Identify the preparation type.
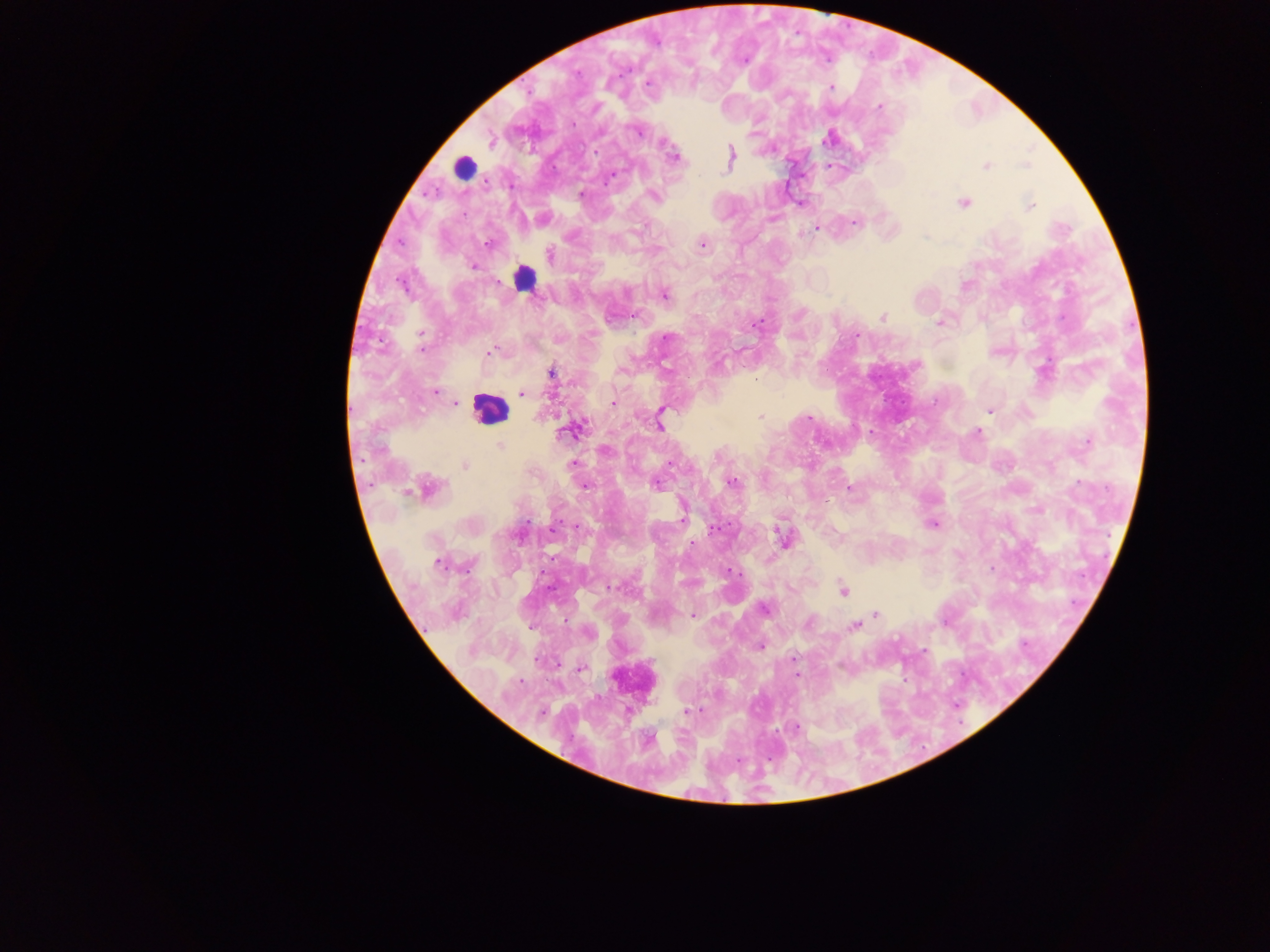

Thick blood film.

Approximate centers as {x, y} in pixels.
Summary:
  - Malaria parasite locations: {648, 82}, {831, 87}, {879, 107}, {636, 132}, {827, 139}, {595, 152}, {731, 156}, {673, 158}, {1025, 165}, {986, 167}, {612, 176}, {582, 194}, {654, 195}, {964, 203}, {800, 204}, {1031, 206}, {855, 223}, {816, 228}, {488, 244}, {702, 244}, {550, 255}, {473, 267}, {965, 285}, {665, 295}, {634, 317}, {883, 317}, {938, 323}, {756, 325}, {421, 335}, {856, 336}, {665, 338}, {421, 348}, {491, 351}, {551, 372}, {436, 391}, {522, 393}, {612, 402}, {455, 403}, {989, 411}, {661, 414}, {760, 417}, {809, 418}, {659, 423}, {567, 431}, {977, 433}, {1087, 444}, {500, 445}, {465, 465}, {731, 483}, {656, 484}, {1079, 484}, {585, 486}, {429, 489}, {850, 489}, {682, 517}, {933, 524}, {712, 530}, {783, 537}, {438, 564}, {729, 570}, {612, 587}, {843, 590}, {765, 608}, {876, 614}, {693, 616}, {809, 622}, {853, 626}, {760, 647}, {923, 651}, {794, 658}, {581, 669}, {796, 676}, {520, 681}, {687, 711}, {541, 712}, {797, 727}
  - Leukocyte locations: {463, 167}, {524, 278}, {489, 409}
  - Image size: 1270×952 pixels
  - Capture: mobile-phone photograph through a microscope
  - Field of view: single
  - Country: Ghana